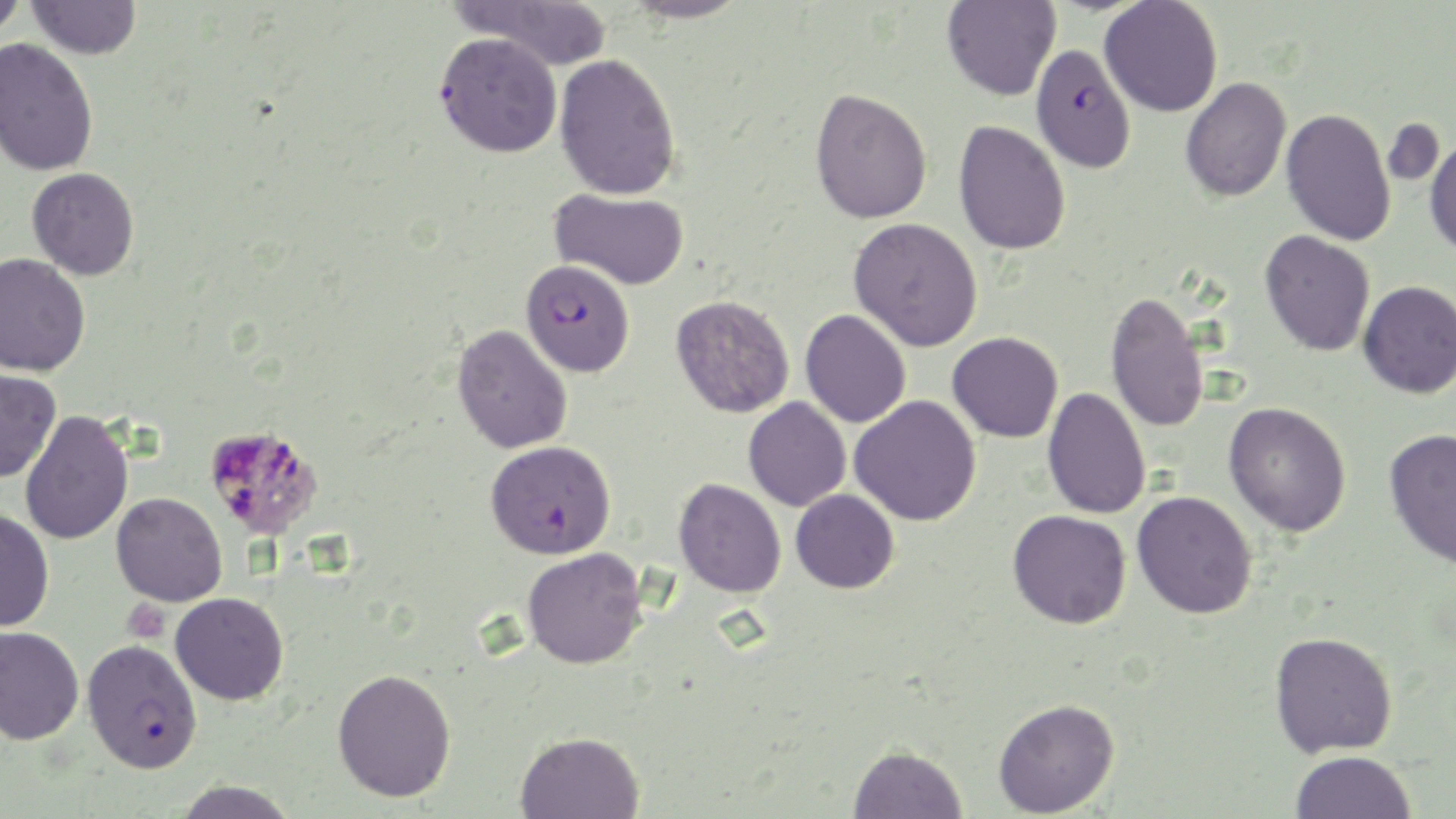 Approximate bounding boxes as [x1, y1, x2, y2] in pixels. Plasmodium falciparum-infected red blood cell locations: [1031, 36, 1137, 167], [520, 258, 635, 377], [486, 440, 615, 559], [81, 639, 202, 774]. Platelet locations: [203, 423, 324, 540], [122, 598, 170, 643]. Uninfected red blood cell locations: [0, 0, 27, 41], [27, 0, 141, 59], [453, 0, 611, 72], [623, 0, 749, 24], [1099, 0, 1223, 117], [942, 1, 1061, 101], [435, 32, 563, 157], [0, 38, 99, 177], [555, 53, 680, 200], [1180, 77, 1292, 202], [809, 87, 932, 224], [1281, 108, 1397, 246], [953, 120, 1071, 255], [1426, 136, 1456, 258], [27, 167, 139, 280], [550, 188, 689, 290], [849, 217, 983, 351], [1260, 230, 1375, 356], [0, 252, 91, 377], [1358, 280, 1456, 398], [1105, 291, 1210, 433], [671, 295, 794, 418], [800, 309, 911, 428], [453, 323, 573, 454], [948, 332, 1063, 443], [0, 367, 61, 483], [1042, 387, 1151, 519], [849, 395, 981, 526], [743, 397, 851, 512], [1223, 401, 1351, 536], [19, 410, 134, 545], [1383, 427, 1456, 569], [673, 478, 786, 597], [791, 489, 899, 593], [1132, 491, 1257, 619], [112, 492, 227, 606], [0, 509, 55, 632], [1008, 509, 1131, 628], [522, 548, 647, 669], [170, 592, 289, 705], [0, 626, 84, 745], [1269, 630, 1397, 757], [332, 668, 456, 803], [993, 698, 1120, 817], [516, 731, 643, 819], [848, 744, 968, 819], [1291, 750, 1416, 819], [172, 780, 299, 819]. Slide-level diagnosis: Plasmodium falciparum. Thin blood film. May-Grünwald-Giemsa stain. Image is 1456×819 pixels. 1000x magnification. One field of a larger specimen. Light microscopy.